Assess the morphology of the erythrocytes.
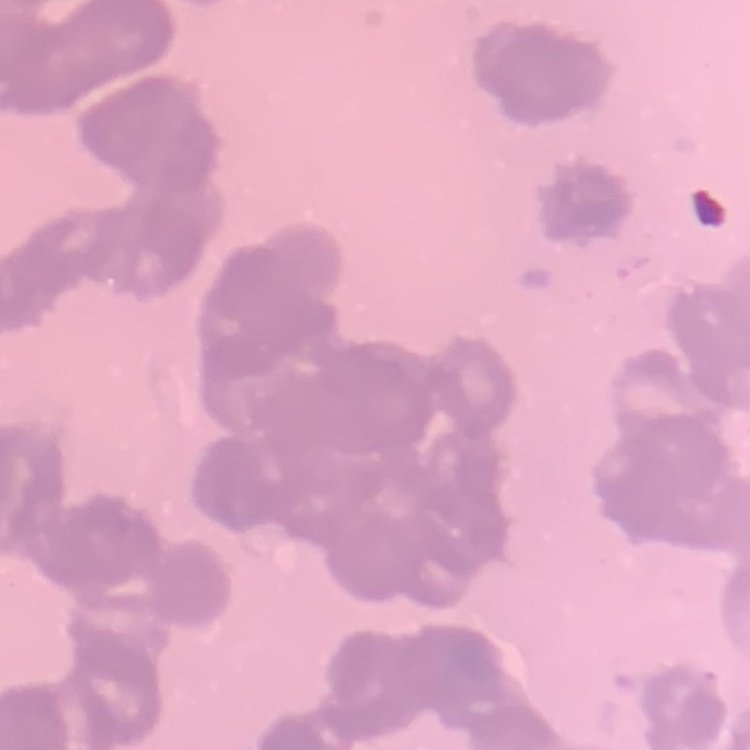
Rouleaux formation.

Square crop of a larger photomicrograph. Field's or Giemsa stain. Thin peripheral smear.